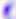
Toxoplasma gondii is shown. Photomicrograph. Captured at 400x magnification.